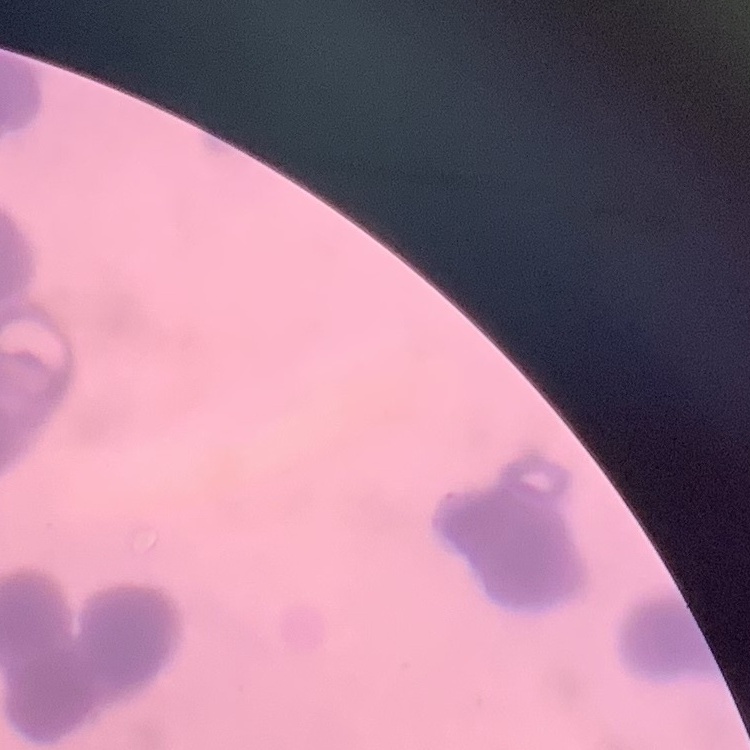
The red blood cells exhibit rouleaux formation. One tile cut from a larger photomicrograph. Thin blood film. Field's or Giemsa stain.